Comment on the morphology of the red blood cells.
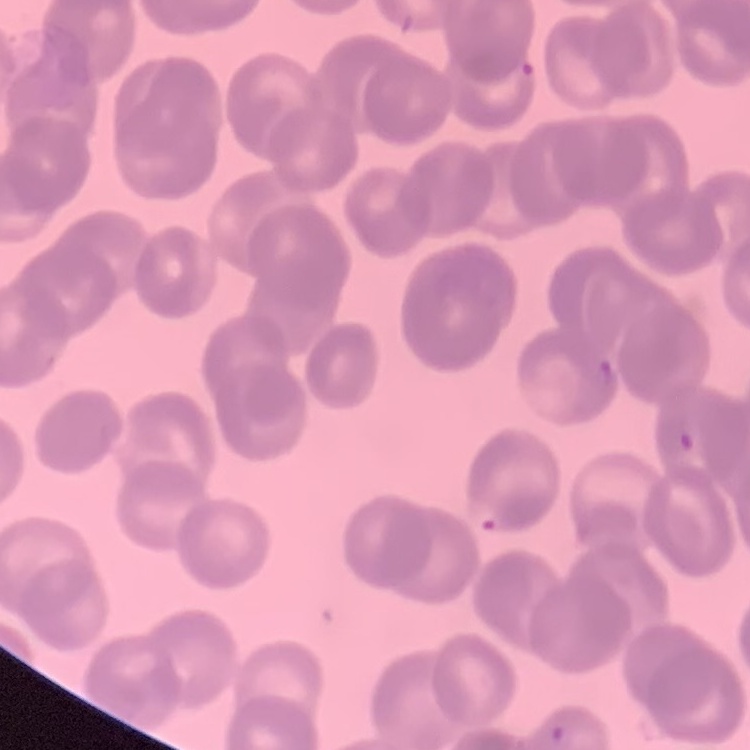
Rouleaux formation.

Summary:
  - Preparation: thin blood film
  - Stain: Field's or Giemsa
  - Image type: square crop of a larger photomicrograph